Identify the parasite.
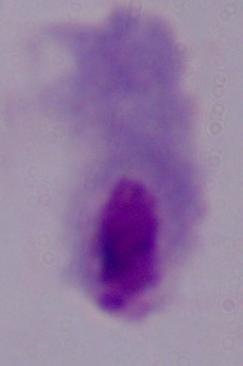
A trichomonad.

modality = photomicrograph
magnification = 1000x